State which parasite is depicted.
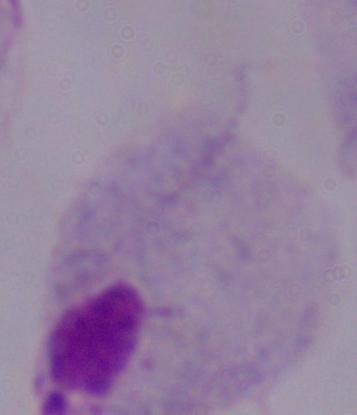

A trichomonad.

modality: micrograph
magnification: 1000x